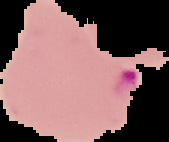
{
  "preparation": "thin blood smear",
  "malaria_status": "parasitized",
  "image_size": "169×142 pixels",
  "image_type": "segmented cell region on a black background"
}